Report the malaria status of this cell.
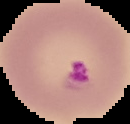

It is parasitized.

From a thin blood film. Image is 130×124 pixels. Segmented cell region on a black background.